Assess the morphology of the red blood cells.
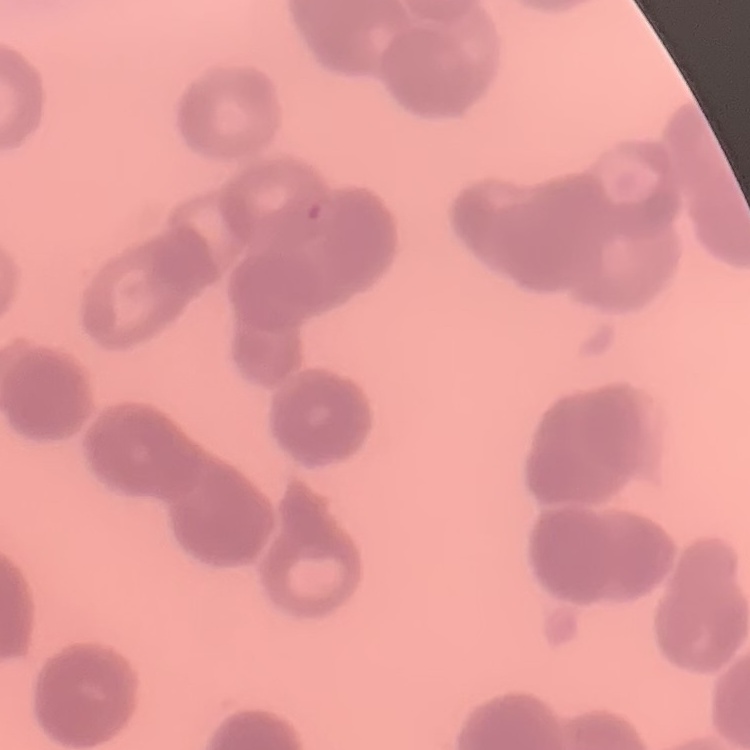
They show rouleaux formation.

Thin peripheral smear. Stained with either Field's or Giemsa. Square crop of a larger photomicrograph.